Assess this cell for malaria.
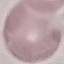

It is uninfected.

Automatically extracted cell patch, resized to 64 × 64 pixels. Thin smear of blood. Giemsa stain. Acquired by smartphone through the microscope eyepiece.